Identify the blood parasite species.
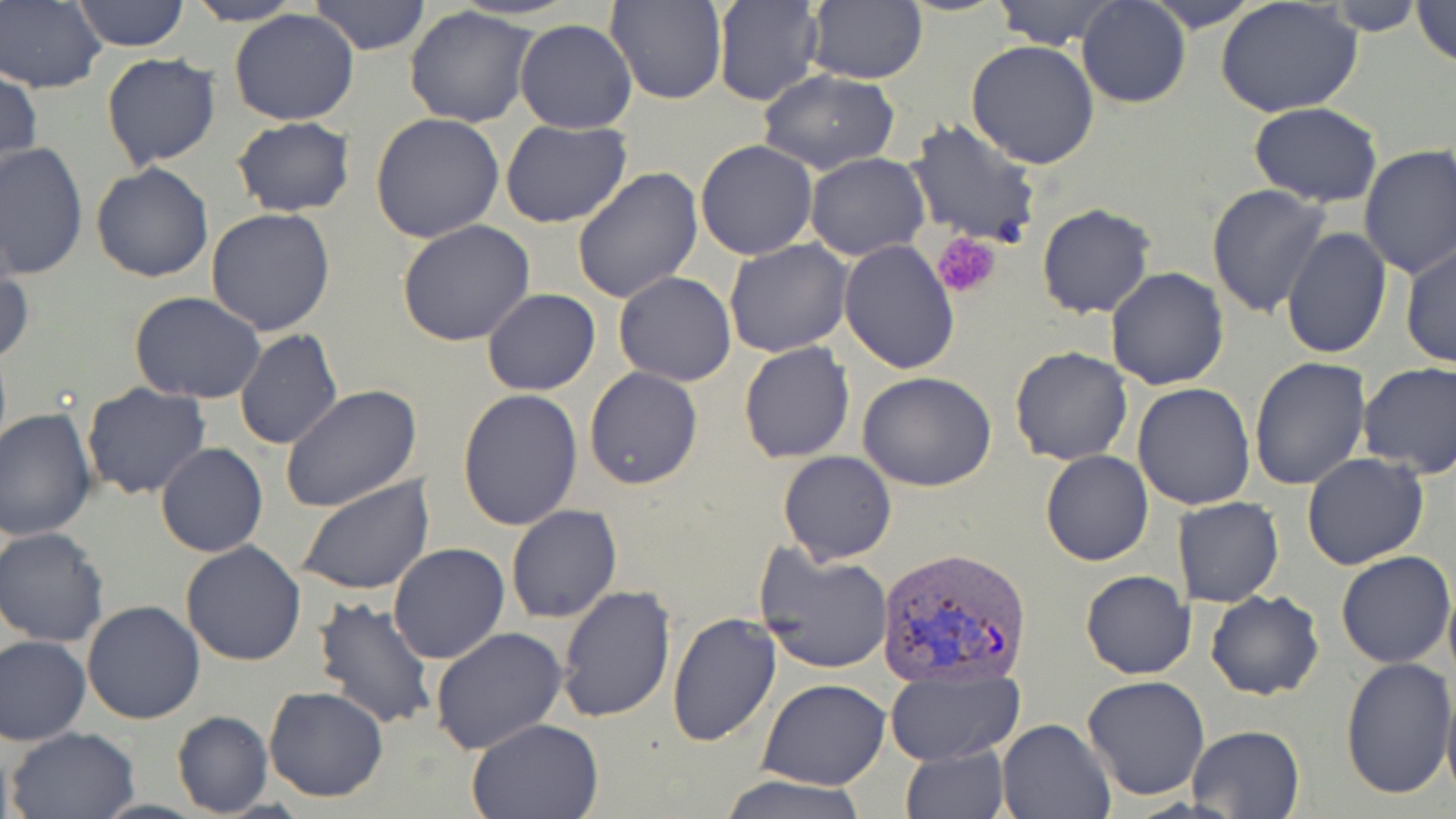

Plasmodium vivax.

field of view = single
Plasmodium vivax-infected red blood cell locations = approximate bounding boxes as named x1/y1/x2/y2 corners in pixels: (x1=873, y1=547, x2=1032, y2=688)
preparation = thin blood film
stain = May-Grünwald-Giemsa
magnification = 1000x
uninfected red blood cell locations = approximate bounding boxes as named x1/y1/x2/y2 corners in pixels: (x1=2, y1=0, x2=106, y2=92), (x1=183, y1=0, x2=305, y2=25), (x1=309, y1=0, x2=429, y2=55), (x1=608, y1=0, x2=725, y2=105), (x1=713, y1=0, x2=825, y2=106), (x1=805, y1=0, x2=927, y2=84), (x1=992, y1=0, x2=1121, y2=49), (x1=1079, y1=0, x2=1190, y2=108), (x1=1142, y1=0, x2=1266, y2=31), (x1=1215, y1=0, x2=1364, y2=119), (x1=1412, y1=0, x2=1456, y2=69), (x1=69, y1=1, x2=191, y2=51), (x1=1321, y1=1, x2=1429, y2=34), (x1=404, y1=6, x2=536, y2=128), (x1=229, y1=8, x2=360, y2=126), (x1=514, y1=18, x2=637, y2=134), (x1=967, y1=41, x2=1100, y2=170), (x1=101, y1=53, x2=220, y2=170), (x1=1, y1=66, x2=41, y2=181), (x1=755, y1=71, x2=902, y2=174), (x1=1249, y1=102, x2=1383, y2=206), (x1=370, y1=113, x2=505, y2=244), (x1=231, y1=117, x2=357, y2=217), (x1=501, y1=119, x2=633, y2=230), (x1=907, y1=119, x2=1041, y2=248), (x1=695, y1=139, x2=820, y2=260), (x1=1, y1=143, x2=88, y2=284), (x1=1357, y1=144, x2=1456, y2=280), (x1=805, y1=151, x2=929, y2=260), (x1=91, y1=163, x2=214, y2=282), (x1=573, y1=166, x2=705, y2=304), (x1=1206, y1=183, x2=1332, y2=320), (x1=1036, y1=202, x2=1156, y2=319), (x1=205, y1=208, x2=336, y2=336), (x1=396, y1=221, x2=536, y2=347), (x1=1281, y1=226, x2=1392, y2=360), (x1=724, y1=239, x2=852, y2=356), (x1=839, y1=240, x2=959, y2=374), (x1=1401, y1=243, x2=1455, y2=370), (x1=0, y1=260, x2=34, y2=370), (x1=1105, y1=266, x2=1230, y2=390), (x1=613, y1=272, x2=738, y2=386), (x1=482, y1=288, x2=600, y2=396), (x1=131, y1=292, x2=264, y2=403), (x1=233, y1=329, x2=343, y2=451), (x1=738, y1=340, x2=854, y2=462), (x1=1009, y1=346, x2=1132, y2=465), (x1=1248, y1=355, x2=1369, y2=490), (x1=1358, y1=361, x2=1456, y2=478), (x1=584, y1=367, x2=702, y2=490), (x1=857, y1=372, x2=997, y2=493), (x1=81, y1=381, x2=211, y2=501), (x1=1132, y1=382, x2=1256, y2=510), (x1=282, y1=385, x2=422, y2=514), (x1=457, y1=388, x2=583, y2=531), (x1=0, y1=408, x2=98, y2=540), (x1=156, y1=442, x2=268, y2=558), (x1=1040, y1=450, x2=1154, y2=566), (x1=777, y1=451, x2=896, y2=564), (x1=1302, y1=452, x2=1429, y2=571), (x1=297, y1=475, x2=434, y2=596), (x1=1180, y1=495, x2=1284, y2=608), (x1=505, y1=505, x2=623, y2=623), (x1=0, y1=529, x2=109, y2=647), (x1=181, y1=541, x2=308, y2=667), (x1=388, y1=542, x2=510, y2=664), (x1=755, y1=546, x2=892, y2=675), (x1=1336, y1=550, x2=1454, y2=667), (x1=1080, y1=570, x2=1195, y2=678), (x1=556, y1=584, x2=675, y2=724), (x1=1205, y1=589, x2=1325, y2=700), (x1=312, y1=595, x2=438, y2=730), (x1=79, y1=600, x2=205, y2=724), (x1=667, y1=612, x2=782, y2=747), (x1=429, y1=627, x2=569, y2=755), (x1=1, y1=636, x2=90, y2=745), (x1=1338, y1=657, x2=1455, y2=800), (x1=886, y1=667, x2=1024, y2=763), (x1=1083, y1=675, x2=1210, y2=801), (x1=758, y1=678, x2=889, y2=789), (x1=263, y1=686, x2=389, y2=802), (x1=1441, y1=686, x2=1456, y2=801), (x1=171, y1=710, x2=273, y2=817), (x1=468, y1=717, x2=605, y2=818), (x1=996, y1=718, x2=1116, y2=818), (x1=1186, y1=724, x2=1306, y2=818), (x1=6, y1=725, x2=141, y2=819), (x1=901, y1=745, x2=1010, y2=819), (x1=716, y1=774, x2=869, y2=819)
image size = 1456×819 pixels
platelet locations = approximate bounding boxes as named x1/y1/x2/y2 corners in pixels: (x1=934, y1=232, x2=1004, y2=299)
modality = light microscopy